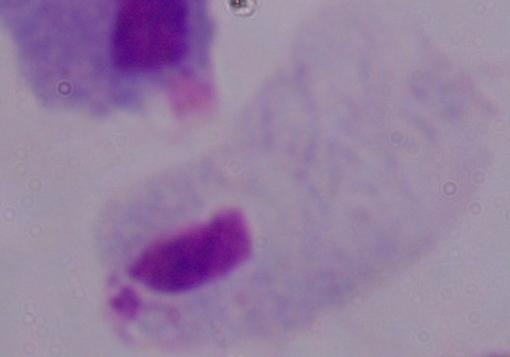

1000x magnification. A trichomonad is seen. Micrograph.